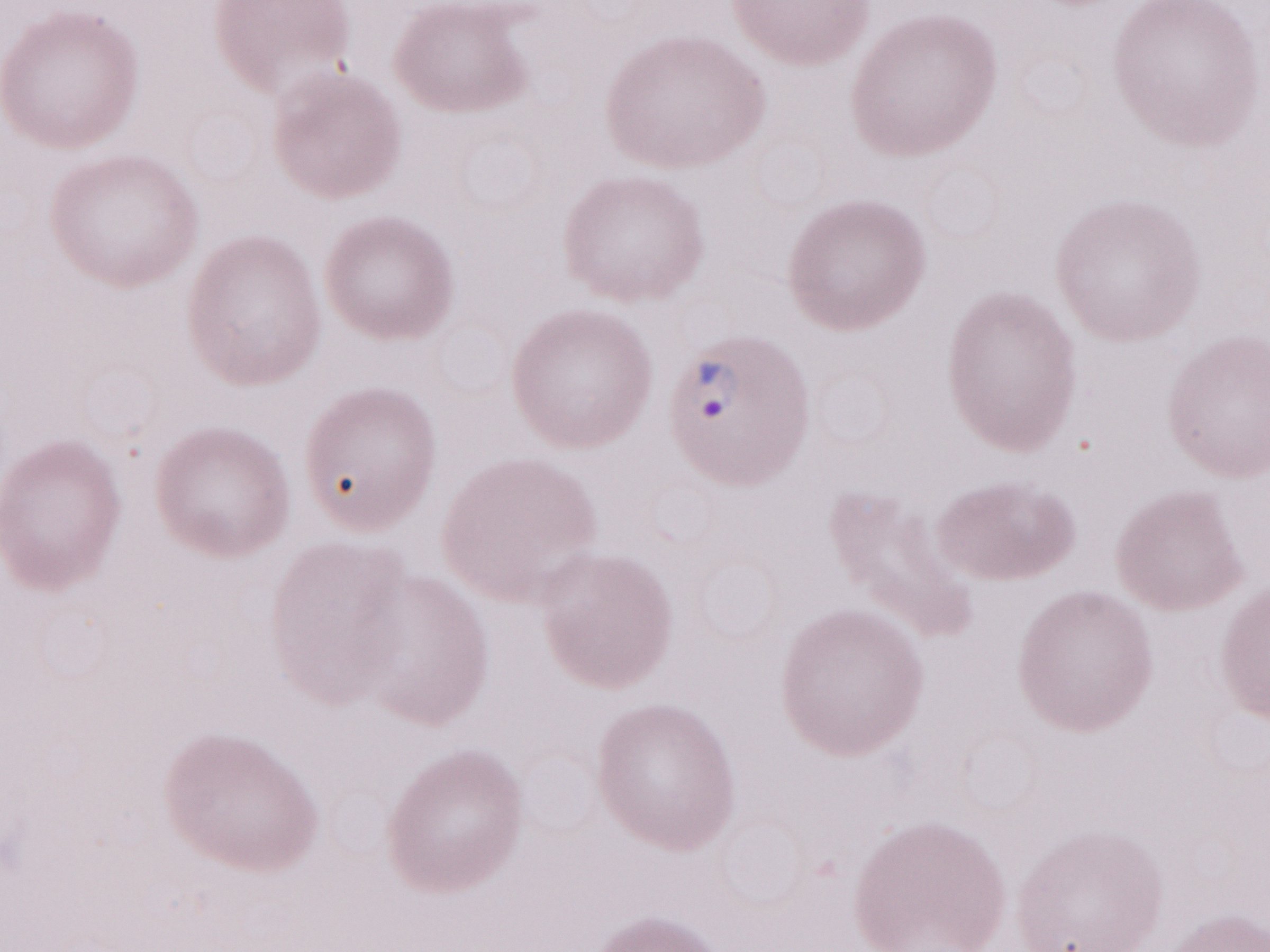 Thin peripheral-blood smear. Image is 1270×952 pixels. Magnification: 1,000x. May-Grünwald-Giemsa (MGG) stain. Malaria diagnosis (patient-level): positive. Olympus BX43 microscope, Olympus DP73 camera. Single field of view.